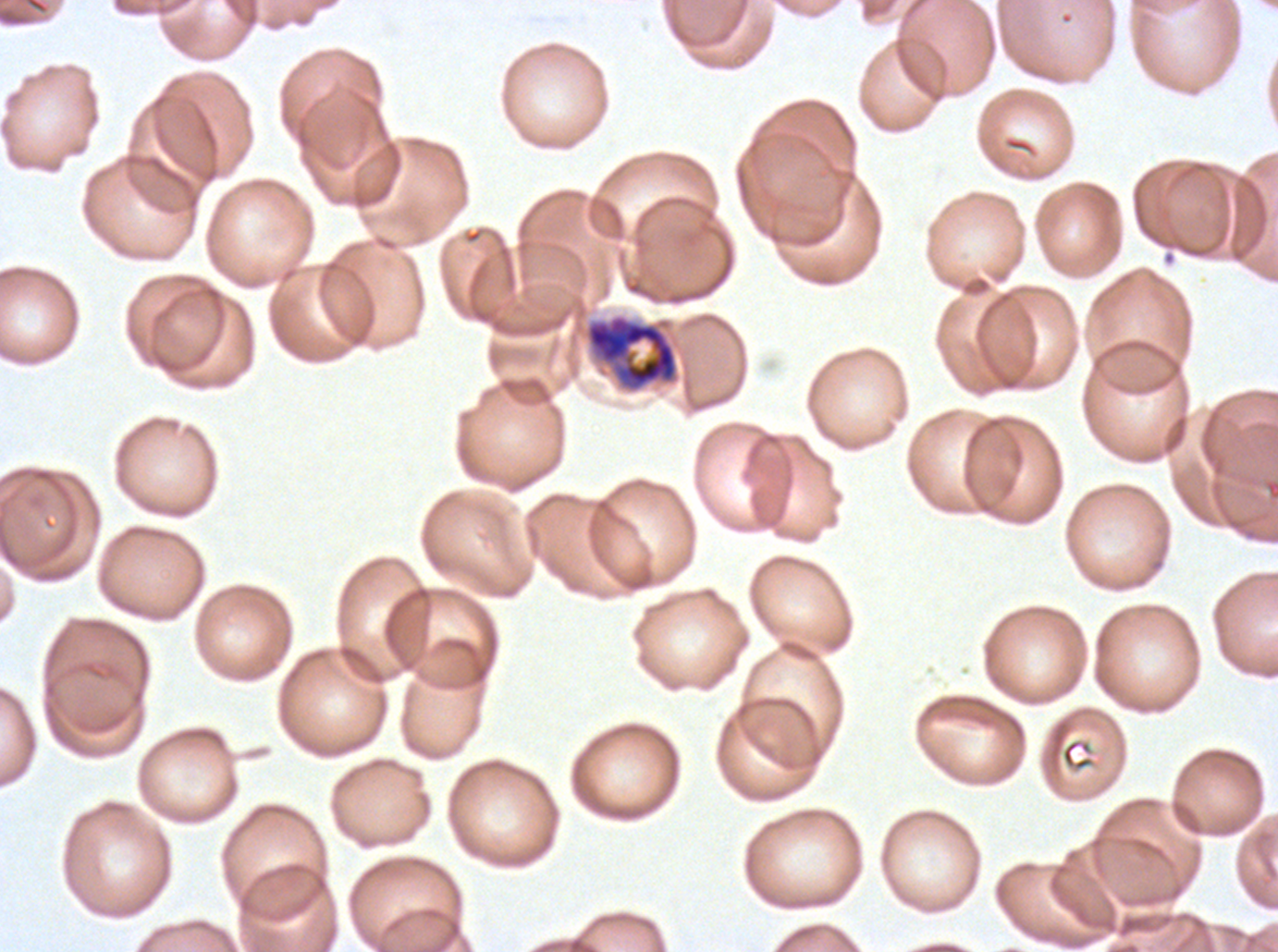

Approximate bounding rectangles given as corner coordinates in pixels from the top-left.
Summary:
  - Late schizont locations: (x1=584, y1=313, x2=680, y2=394)
  - Specimen: Plasmodium falciparum cultured ex vivo for 24 to 48 hours, from a patient in The Gambia
  - Stain: Giemsa
  - Field of view: sub-image separated from a larger composite
  - Image size: 1278×952 pixels
  - Preparation: thin blood film